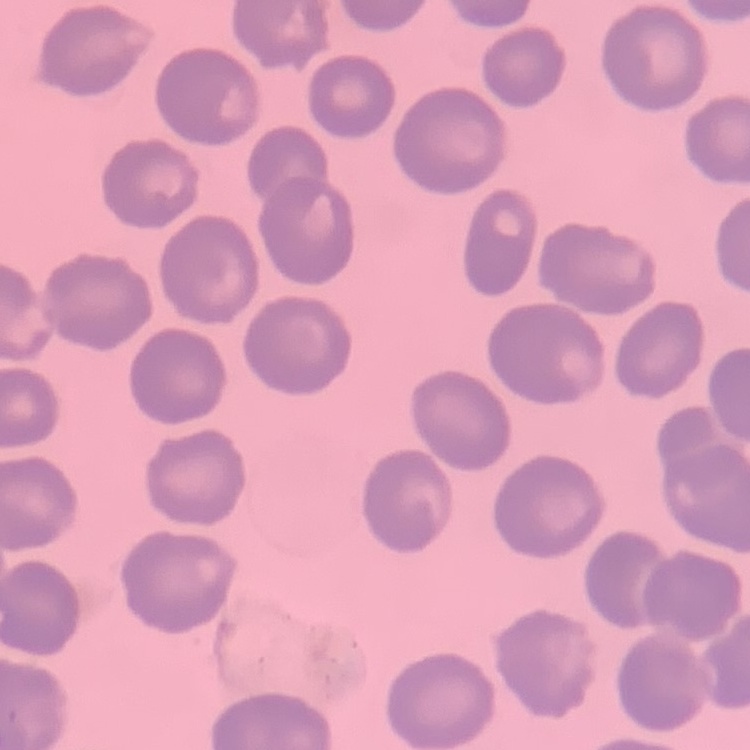
red_blood_cell_morphology: no rouleaux formation
preparation: thin blood film
stain: Field's or Giemsa
image_type: square crop of a larger photomicrograph